Assess the morphology of the erythrocytes.
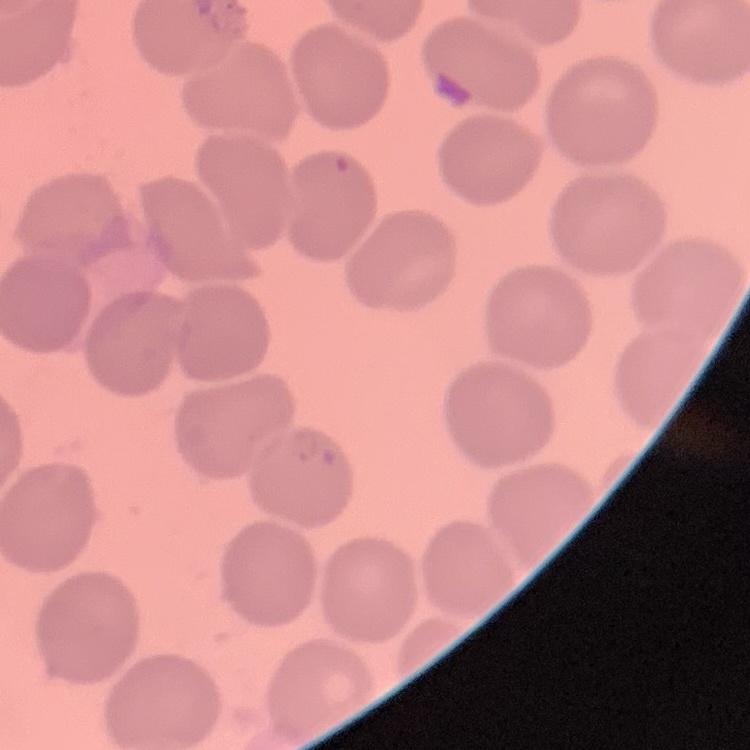

No rouleaux formation.

preparation = thin blood smear
image type = square crop of a larger photomicrograph
stain = Field's or Giemsa